Give the position of every leukocyte visible.
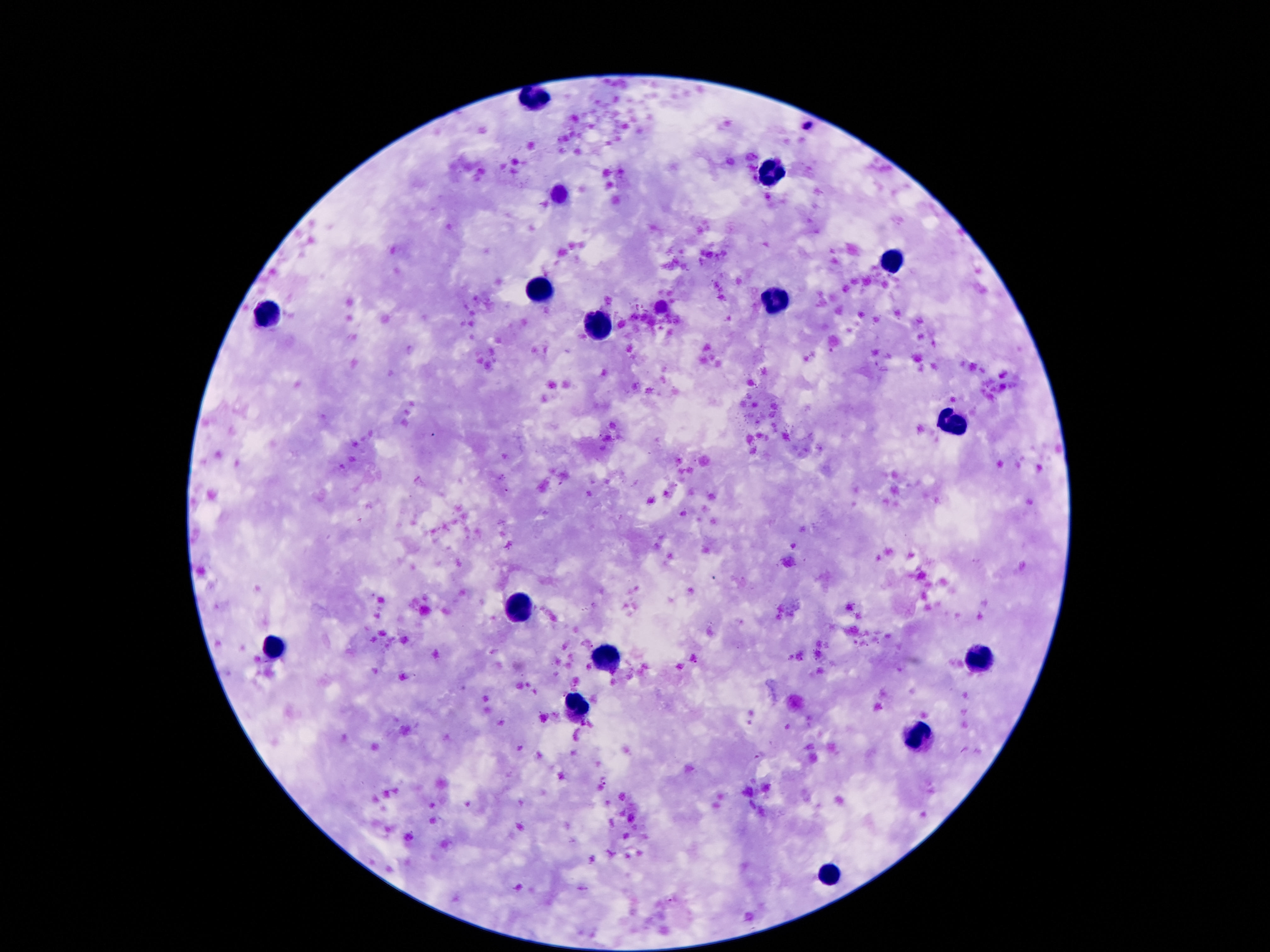
Approximate centers as {x, y} in pixels.
Leukocytes: {529, 98}, {769, 168}, {891, 260}, {537, 290}, {775, 300}, {265, 314}, {597, 326}, {951, 420}, {519, 608}, {271, 646}, {607, 654}, {981, 654}, {577, 704}, {919, 738}, {831, 874}.

Patient malaria status: uninfected. Image is 1270×952 pixels. Photographed through the microscope eyepiece with a smartphone camera. 100x magnification. Giemsa stain. One field from this slide. Thick blood film.